Classify this cell by malaria status.
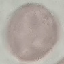
It is uninfected.

preparation = thin blood smear
image type = cell patch, automatically extracted from a larger field of view and resized to 64 × 64 pixels
capture = smartphone camera at the microscope eyepiece
stain = Giemsa